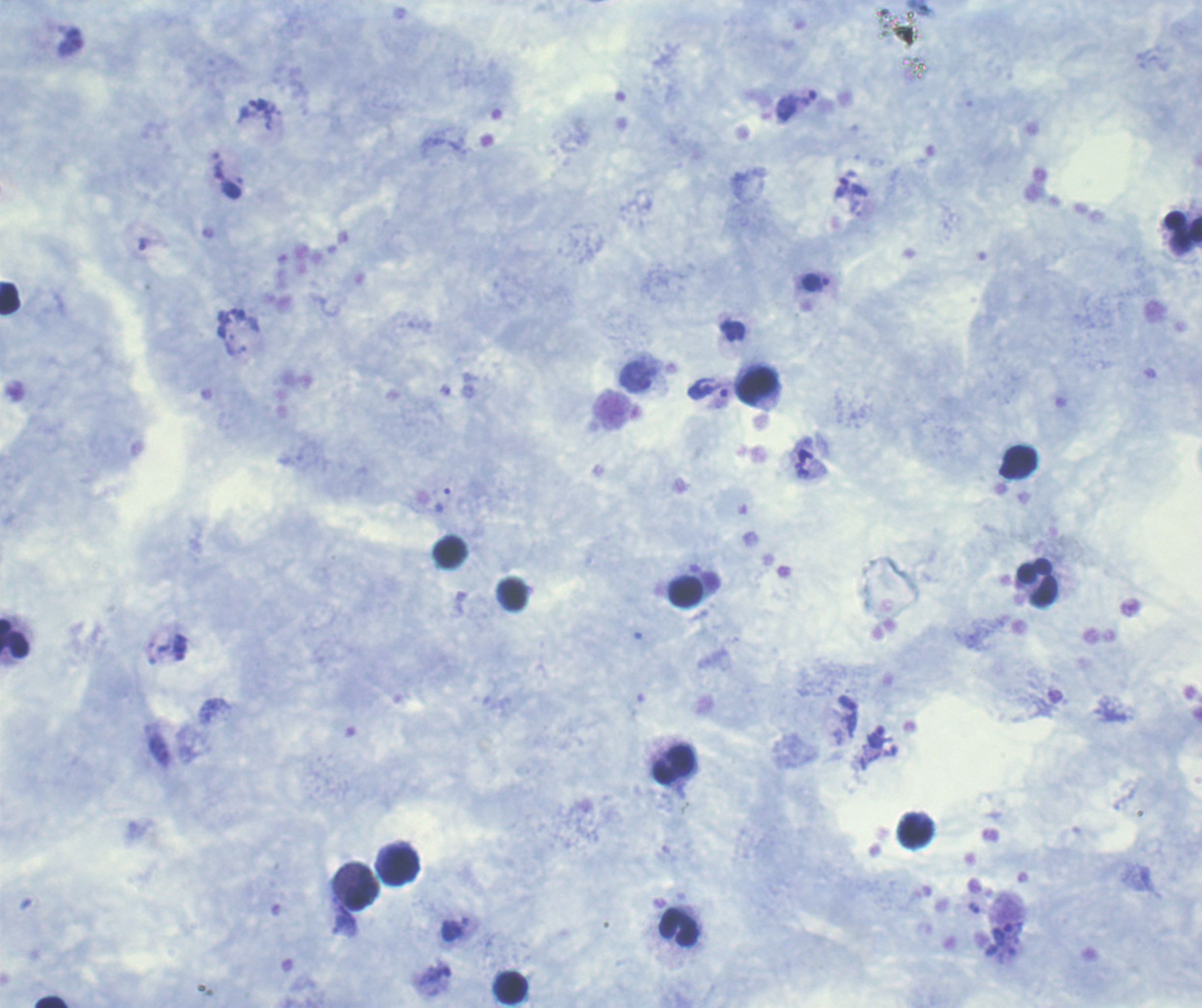

Approximate centers as (x, y) in pixels. Leukocyte locations: (1183, 231), (10, 298), (758, 387), (449, 551), (1038, 582), (686, 592), (14, 639), (675, 766), (916, 832), (400, 866), (362, 890), (679, 927), (511, 988), (50, 1002). Trophozoite locations: (72, 42), (228, 186), (841, 187), (816, 282), (733, 332), (708, 389), (181, 652), (875, 737), (974, 909). One field from this slide. Coloration quality: good. Background quality: satisfactory. Romanowsky-stained preparation. Result: positive for Plasmodium parasites. Thick blood film. Previously used in a real diagnosis. Image is 1202×1008 pixels. Captured at 100x magnification.